Locate every Plasmodium parasite.
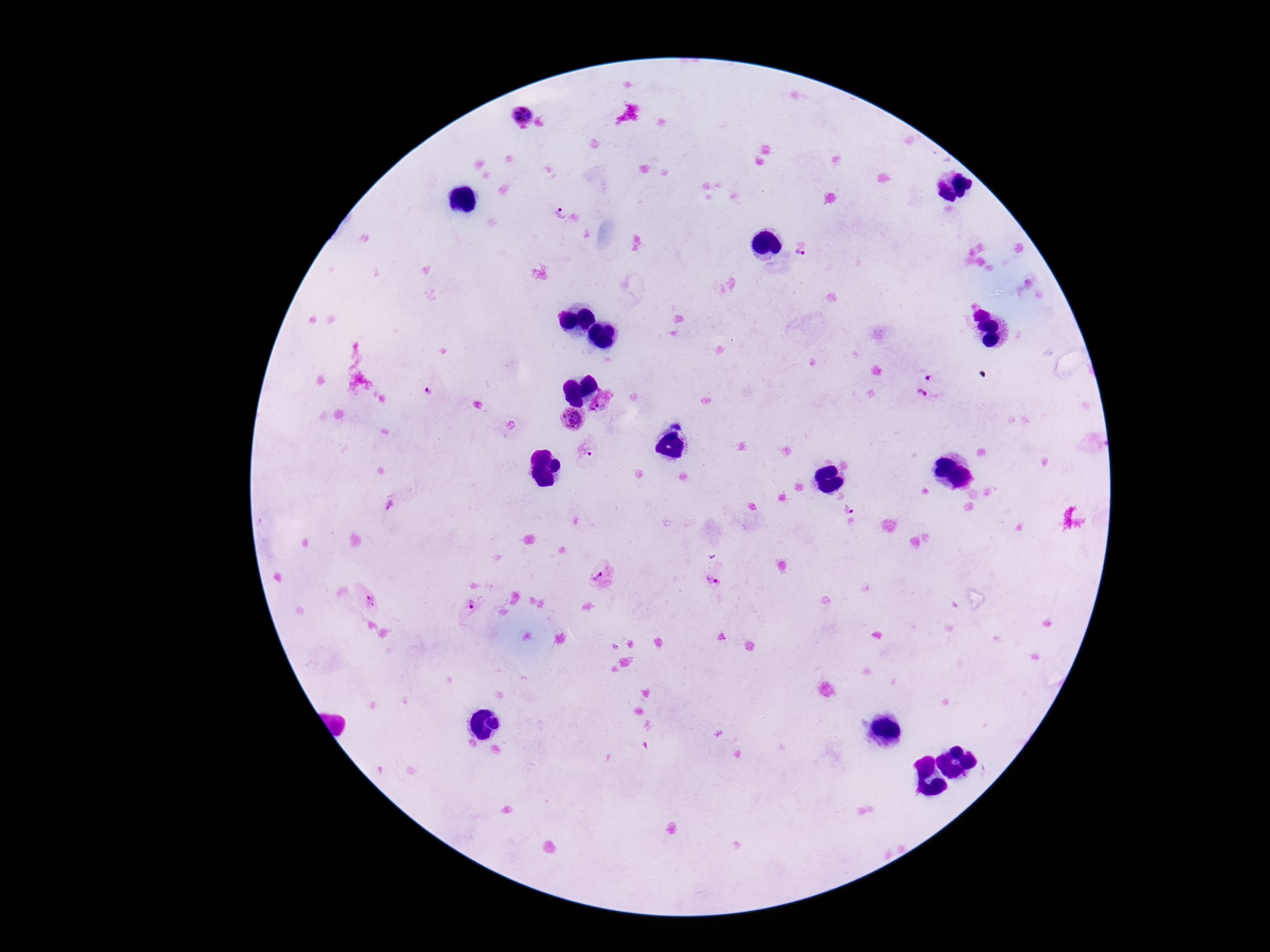
Approximate centers as [x, y] in pixels.
Plasmodium parasites: [520, 116], [559, 215], [808, 249], [928, 378], [429, 392], [921, 394], [601, 408], [571, 420], [585, 451], [393, 506], [846, 506], [601, 577], [713, 580], [369, 599], [469, 608].

image size = 1270×952 pixels
stain = Giemsa
capture = smartphone camera through the microscope eyepiece
preparation = thick blood film
patient malaria status = infected
magnification = 100x
field of view = single